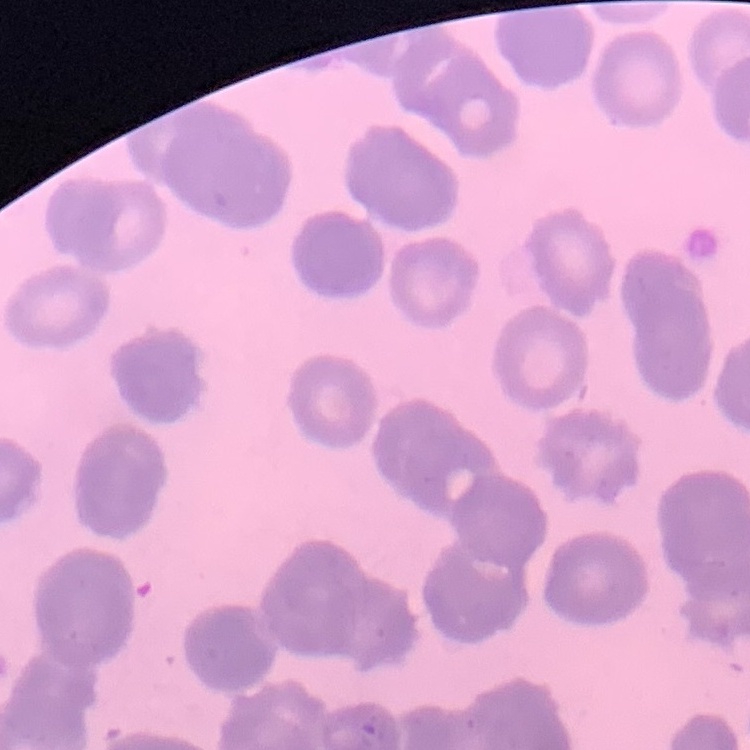
red blood cell morphology = rouleaux formation
stain = Field's or Giemsa
preparation = thin blood film
image type = one tile cut from a larger photomicrograph